Identify the blood parasite species.
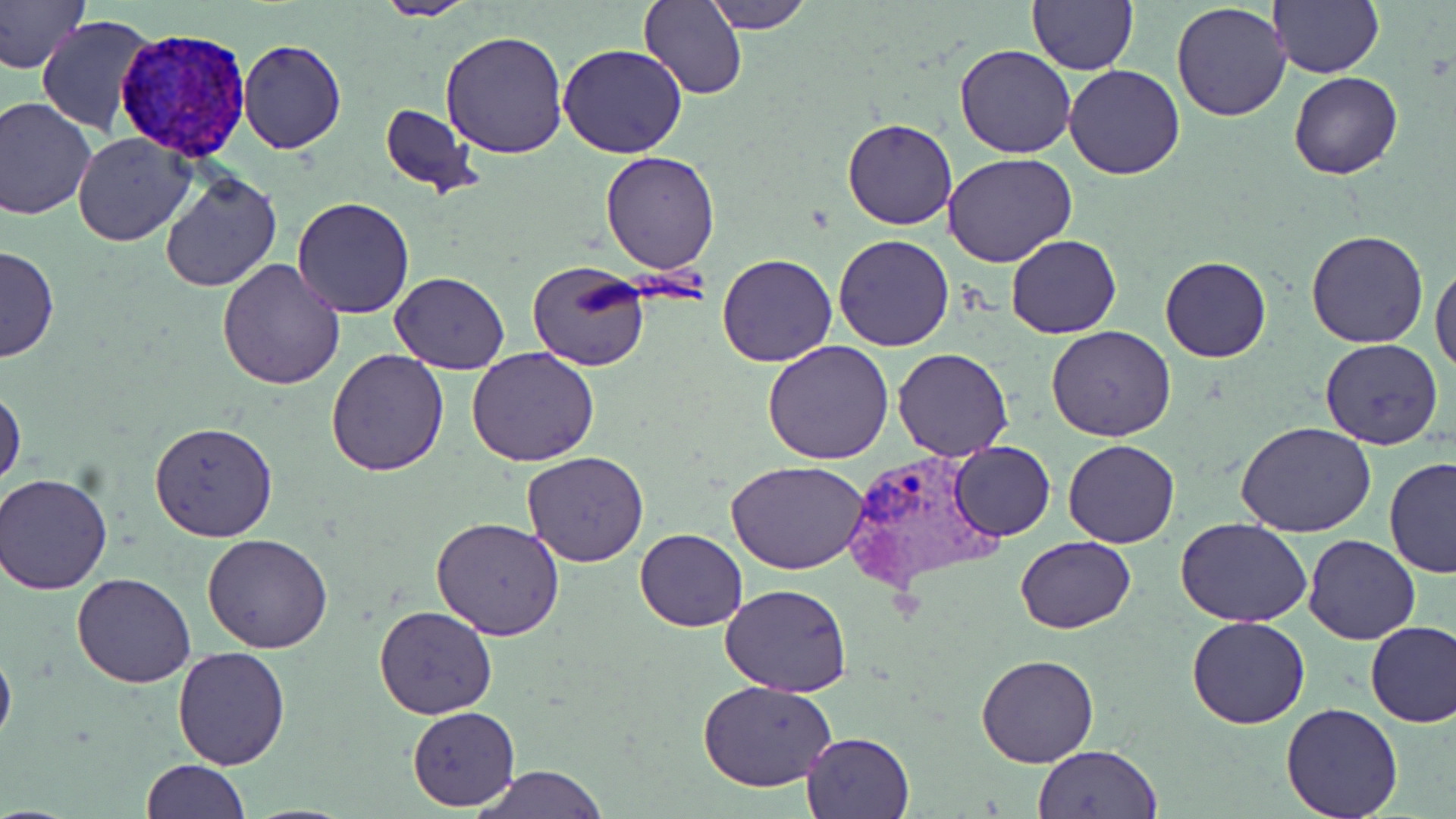

Plasmodium vivax.

Approximate bounding boxes as named x1/y1/x2/y2 corners in pixels. Plasmodium vivax-infected red blood cell locations: (x1=118, y1=31, x2=247, y2=166), (x1=843, y1=449, x2=1005, y2=591). Uninfected red blood cell locations: (x1=0, y1=0, x2=89, y2=74), (x1=373, y1=0, x2=477, y2=21), (x1=641, y1=0, x2=747, y2=101), (x1=705, y1=0, x2=815, y2=31), (x1=1027, y1=0, x2=1139, y2=75), (x1=1269, y1=0, x2=1384, y2=78), (x1=1171, y1=1, x2=1292, y2=121), (x1=37, y1=14, x2=153, y2=136), (x1=439, y1=29, x2=569, y2=158), (x1=238, y1=39, x2=347, y2=154), (x1=557, y1=43, x2=688, y2=160), (x1=953, y1=44, x2=1077, y2=159), (x1=1064, y1=64, x2=1186, y2=180), (x1=1289, y1=70, x2=1402, y2=179), (x1=0, y1=98, x2=97, y2=221), (x1=380, y1=105, x2=478, y2=196), (x1=842, y1=117, x2=958, y2=230), (x1=72, y1=131, x2=195, y2=246), (x1=943, y1=152, x2=1077, y2=268), (x1=600, y1=153, x2=720, y2=275), (x1=157, y1=171, x2=283, y2=293), (x1=291, y1=196, x2=415, y2=319), (x1=1306, y1=229, x2=1431, y2=348), (x1=833, y1=234, x2=956, y2=352), (x1=1007, y1=235, x2=1121, y2=338), (x1=0, y1=245, x2=60, y2=363), (x1=717, y1=253, x2=837, y2=366), (x1=1160, y1=256, x2=1271, y2=363), (x1=218, y1=259, x2=347, y2=390), (x1=527, y1=260, x2=651, y2=373), (x1=1432, y1=260, x2=1456, y2=376), (x1=390, y1=272, x2=511, y2=374), (x1=1047, y1=325, x2=1176, y2=441), (x1=1319, y1=338, x2=1444, y2=450), (x1=762, y1=340, x2=896, y2=464), (x1=892, y1=347, x2=1014, y2=461), (x1=467, y1=348, x2=598, y2=466), (x1=326, y1=350, x2=448, y2=477), (x1=0, y1=386, x2=26, y2=493), (x1=149, y1=420, x2=278, y2=542), (x1=1234, y1=420, x2=1378, y2=536), (x1=1063, y1=438, x2=1180, y2=548), (x1=949, y1=441, x2=1057, y2=541), (x1=522, y1=452, x2=651, y2=568), (x1=1382, y1=456, x2=1456, y2=577), (x1=727, y1=460, x2=869, y2=575), (x1=1, y1=471, x2=113, y2=595), (x1=431, y1=517, x2=565, y2=641), (x1=1177, y1=517, x2=1312, y2=626), (x1=634, y1=529, x2=747, y2=633), (x1=1301, y1=533, x2=1421, y2=644), (x1=202, y1=534, x2=333, y2=654), (x1=1015, y1=536, x2=1137, y2=634), (x1=72, y1=572, x2=195, y2=688), (x1=721, y1=583, x2=852, y2=697), (x1=372, y1=605, x2=497, y2=719), (x1=1187, y1=615, x2=1310, y2=729), (x1=1364, y1=619, x2=1456, y2=728), (x1=0, y1=640, x2=16, y2=753), (x1=172, y1=646, x2=290, y2=769), (x1=976, y1=654, x2=1100, y2=769), (x1=698, y1=680, x2=837, y2=792), (x1=1279, y1=702, x2=1405, y2=819), (x1=408, y1=706, x2=521, y2=810), (x1=800, y1=730, x2=914, y2=818), (x1=1030, y1=744, x2=1162, y2=818), (x1=141, y1=758, x2=249, y2=818), (x1=475, y1=767, x2=609, y2=819). Single field of view. Thin blood smear. May-Grünwald-Giemsa-stained preparation. Optical microscopy. Image is 1456×819 pixels. 1000x magnification.